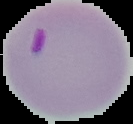

Summary:
  - Result: Plasmodium parasites detected
  - Image size: 133×124 pixels
  - Preparation: thin blood smear
  - Image type: segmented cell region on a black background